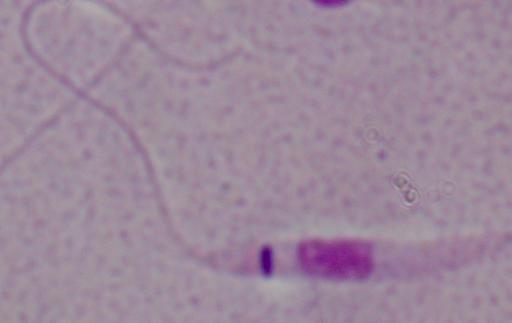
A Leishmania parasite is shown. Micrograph. 1000x magnification.